Name the parasite shown.
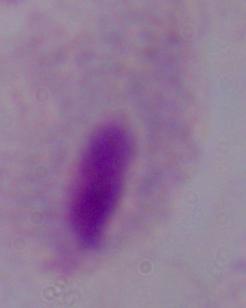
A trichomonad.

Summary:
  - Modality: micrograph
  - Magnification: 1000x